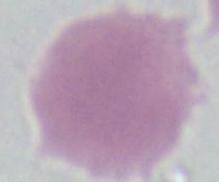 An erythrocyte is shown. Micrograph. 1000x magnification.